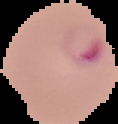
From a thin blood film. Image is 118×124 pixels. Result: malaria parasites identified. Segmented cell region on a black background.